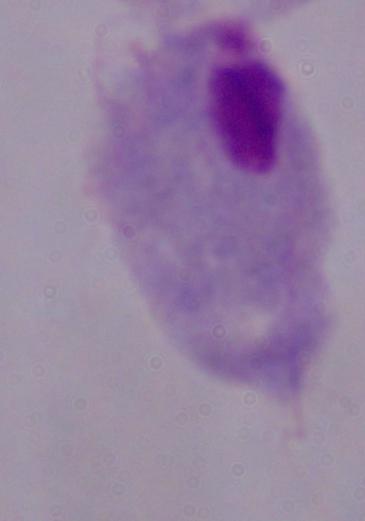
A trichomonad is shown. Micrograph. 1000x magnification.